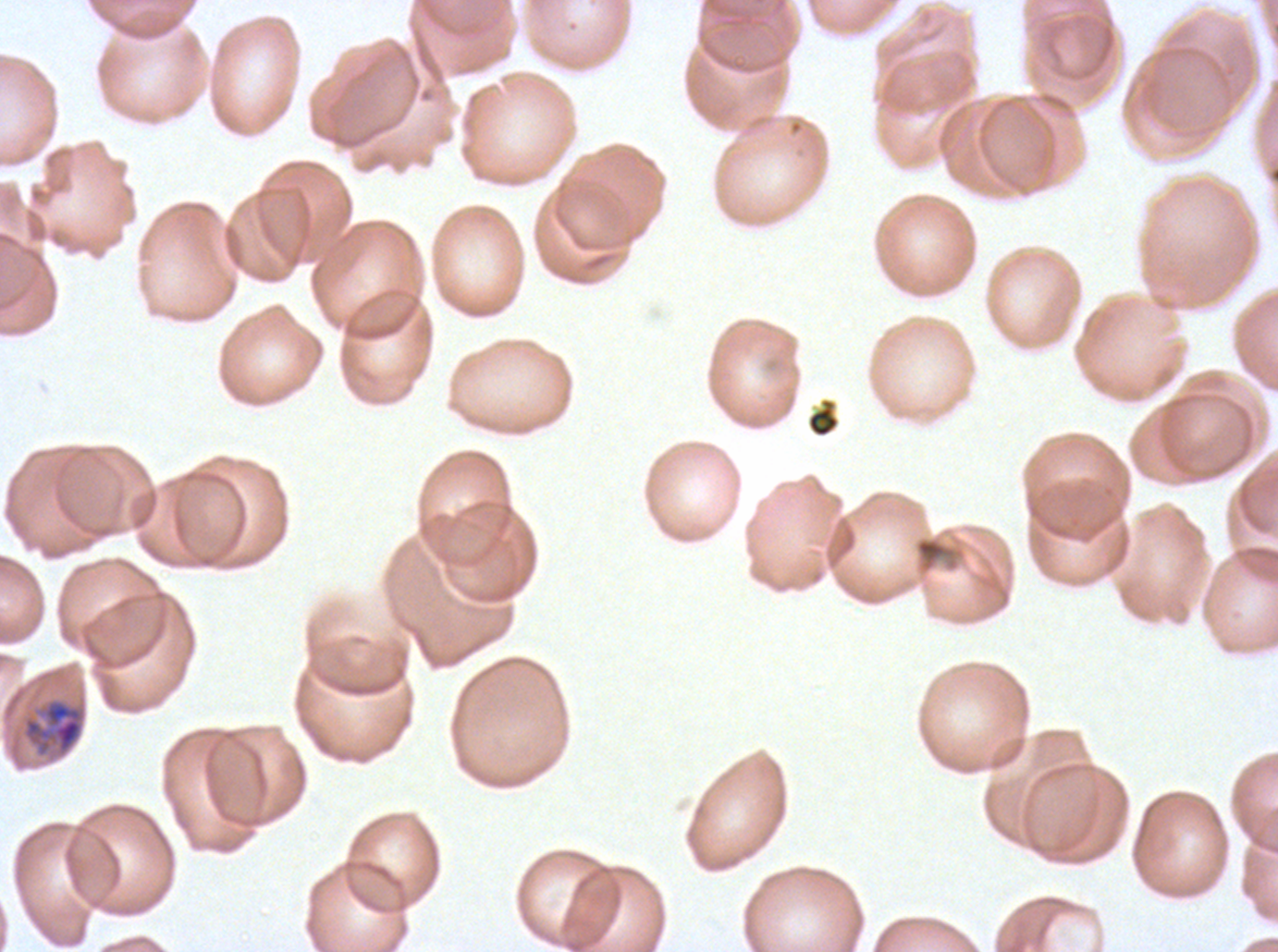

notation = approximate bounding boxes as [x1, y1, x2, y2] in pixels
late trophozoite locations = [20, 696, 88, 761]
debris locations = [806, 397, 840, 438]
specimen = ex-vivo P. falciparum culture from a patient in The Gambia, grown for 24 to 48 hours
preparation = thin blood smear
stain = Giemsa
field of view = one sub-image of a larger composite
image size = 1278×952 pixels